Assess this cell for malaria.
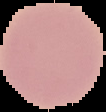

It is uninfected.

The area outside the segmented cell region is set to black. From a thin blood film. Image is 106×112 pixels.